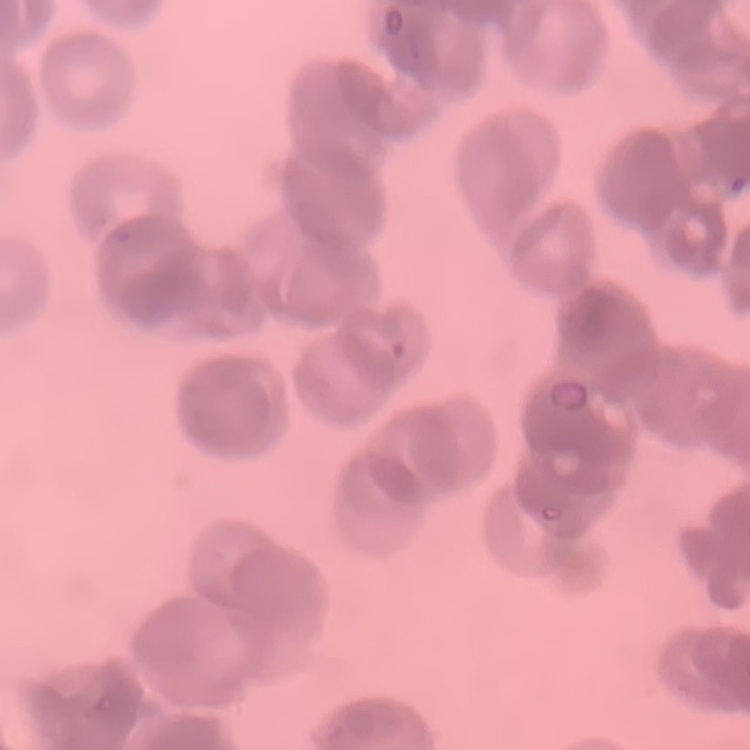 The red blood cells show rouleaux formation. Stained with either Field's or Giemsa. One tile cut from a larger photomicrograph. Thin peripheral smear.